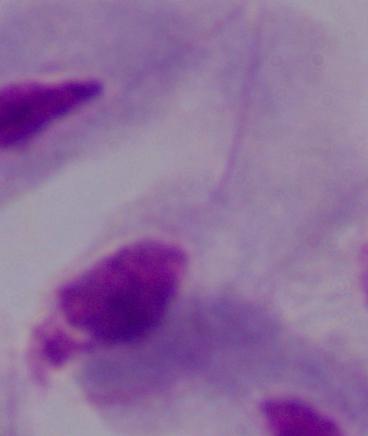
Captured at 1000x magnification. A trichomonad is shown. Micrograph.